Name the parasite shown.
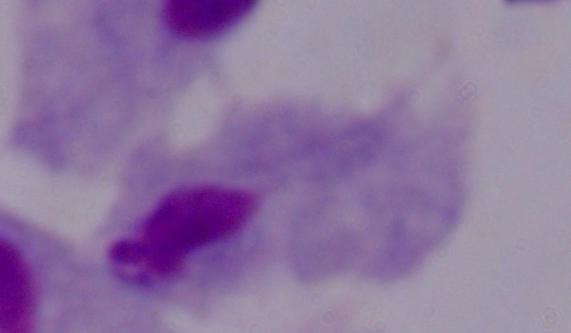

A trichomonad.

{
  "modality": "photomicrograph",
  "magnification": "1000x"
}